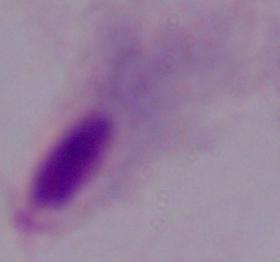

{
  "modality": "photomicrograph",
  "magnification": "1000x",
  "identification": "trichomonad"
}